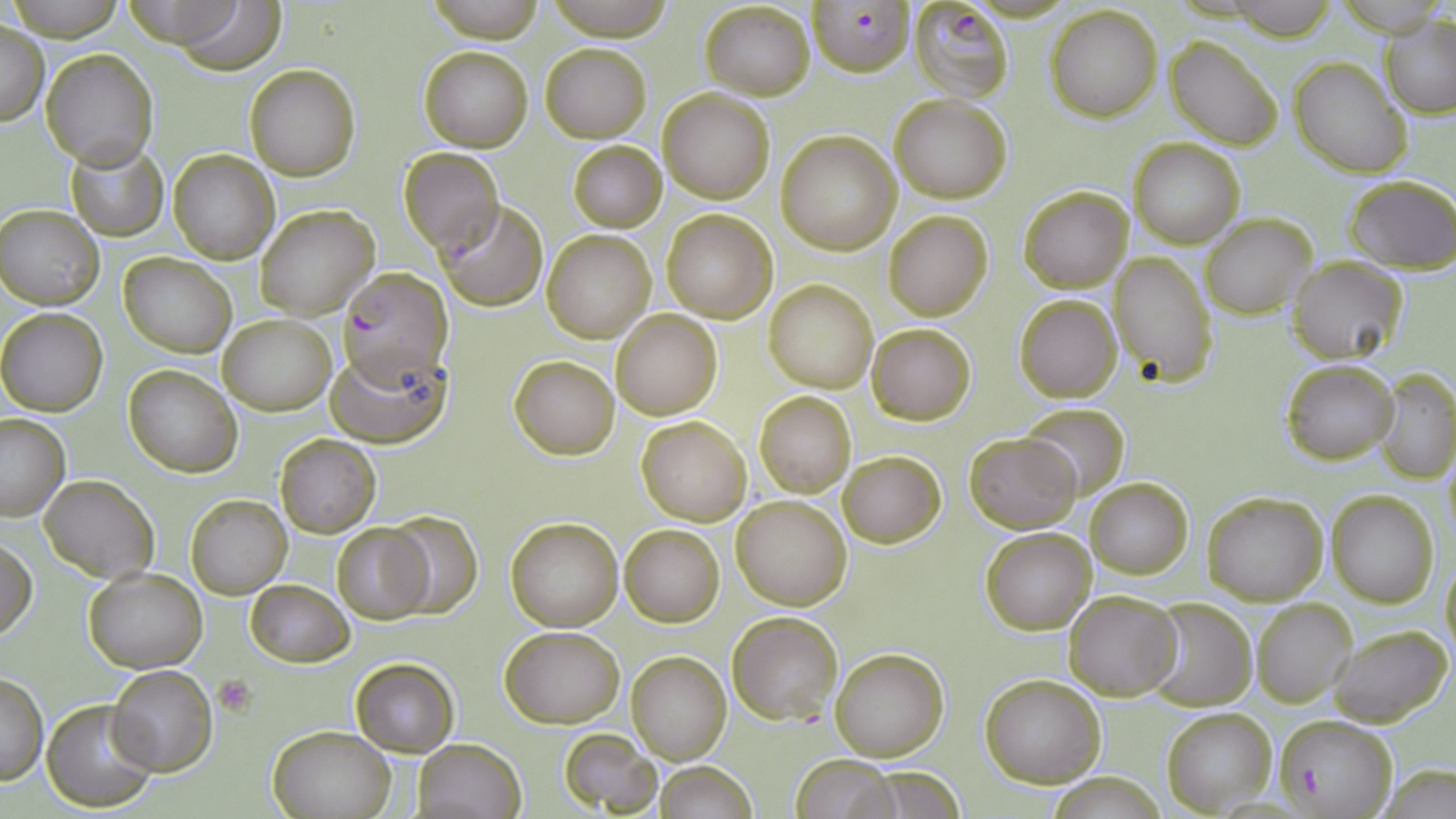 Approximate bounding boxes as (x1, y1, x2, y2) in pixels. Platelet locations: (213, 675, 255, 714). Plasmodium falciparum-infected red blood cell locations: (807, 0, 915, 76), (907, 0, 1014, 103), (337, 267, 453, 382), (1275, 715, 1397, 816). Uninfected red blood cell locations: (6, 0, 126, 37), (117, 0, 254, 49), (428, 0, 545, 44), (544, 0, 678, 38), (170, 2, 285, 74), (1218, 2, 1347, 37), (700, 3, 815, 98), (1044, 5, 1163, 121), (1382, 16, 1456, 119), (1, 22, 48, 125), (1166, 36, 1282, 149), (539, 42, 651, 143), (419, 45, 533, 152), (40, 49, 157, 169), (1290, 57, 1410, 178), (244, 64, 361, 182), (659, 88, 774, 203), (890, 94, 1012, 203), (776, 131, 901, 254), (1129, 138, 1245, 249), (567, 139, 667, 232), (66, 142, 168, 240), (168, 148, 280, 263), (398, 148, 503, 255), (1345, 175, 1456, 272), (1019, 185, 1133, 293), (436, 202, 549, 312), (1, 204, 104, 308), (255, 204, 378, 318), (661, 208, 778, 324), (883, 210, 995, 321), (1200, 213, 1316, 318), (542, 229, 656, 342), (1109, 251, 1219, 387), (120, 253, 235, 356), (1289, 259, 1409, 365), (764, 280, 878, 392), (1014, 294, 1120, 402), (0, 308, 108, 416), (612, 310, 721, 420), (219, 313, 337, 416), (866, 323, 975, 424), (327, 345, 452, 447), (508, 355, 620, 459), (1281, 360, 1398, 464), (123, 365, 242, 477), (1375, 370, 1456, 482), (755, 392, 856, 497), (1018, 403, 1130, 497), (0, 414, 71, 520), (636, 416, 752, 524), (963, 432, 1081, 533), (275, 434, 381, 538), (839, 450, 945, 548), (1443, 452, 1456, 546), (40, 475, 157, 581), (1084, 475, 1193, 581), (1202, 491, 1329, 605), (1327, 492, 1439, 607), (186, 493, 292, 599), (731, 494, 853, 609), (383, 510, 484, 619), (505, 516, 623, 632), (332, 522, 434, 624), (620, 524, 725, 626), (980, 528, 1096, 635), (0, 537, 36, 642), (1440, 558, 1456, 662), (84, 568, 206, 673), (245, 579, 352, 666), (1064, 589, 1183, 700), (1143, 598, 1256, 710), (1251, 600, 1355, 707), (726, 611, 842, 725), (1325, 622, 1453, 728), (500, 626, 625, 728), (830, 647, 948, 762), (627, 651, 730, 763), (351, 658, 458, 756), (108, 665, 218, 776), (0, 671, 48, 784), (980, 674, 1106, 787), (42, 697, 159, 810), (1162, 707, 1277, 815), (268, 723, 397, 818), (558, 729, 663, 814), (413, 738, 526, 819), (791, 754, 900, 819), (653, 761, 757, 819), (1377, 764, 1456, 819), (855, 766, 968, 816), (1047, 773, 1167, 817). Slide-level diagnosis: Plasmodium falciparum. Optical microscopy. Thin blood smear. May-Grünwald-Giemsa-stained preparation. One field of a larger specimen. Image is 1456×819 pixels. Captured at 1000x magnification.